Outline each blood parasite and name the species.
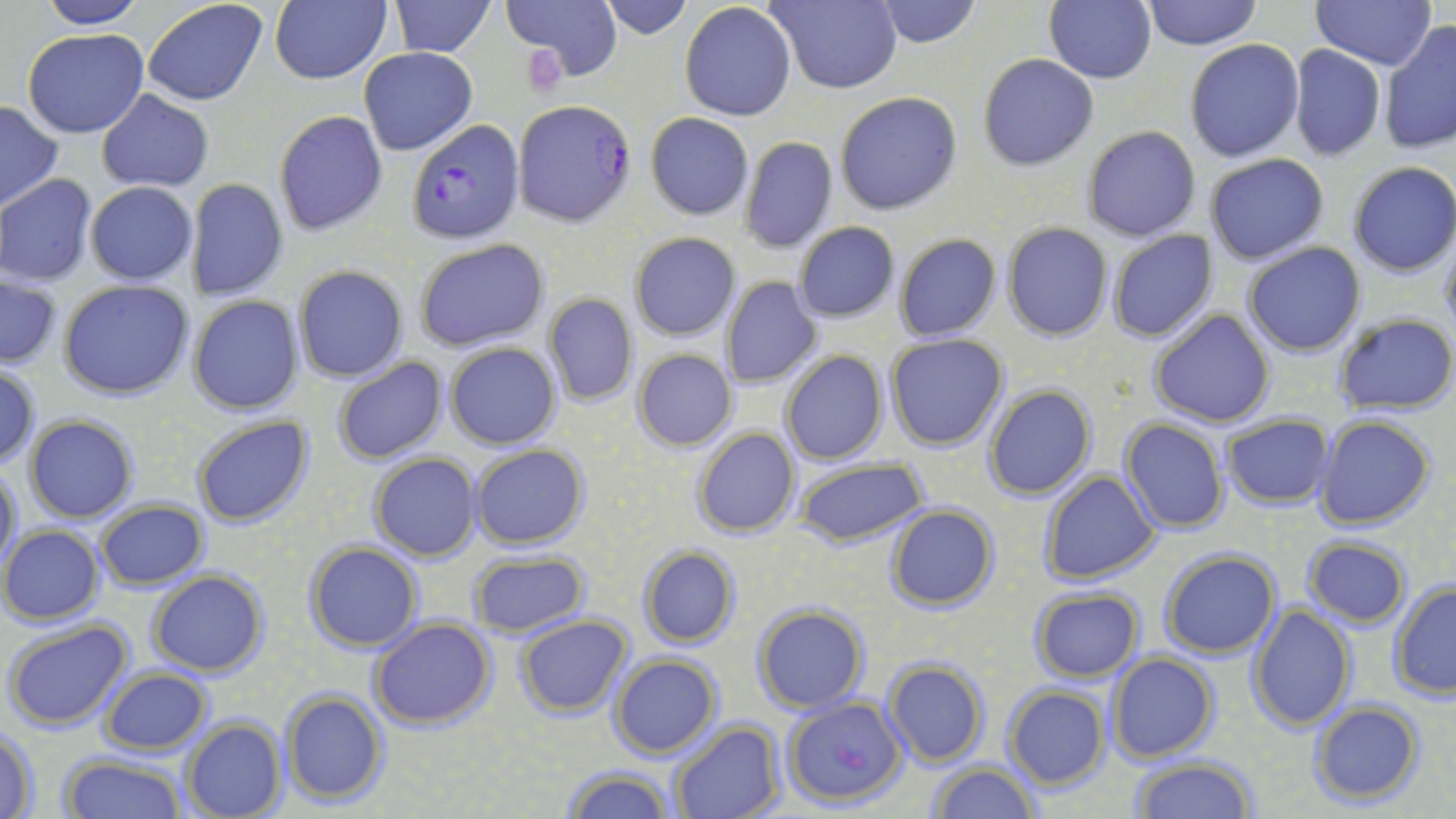

Approximate bounding boxes as (x1, y1, x2, y2) in pixels.
Plasmodium falciparum-infected red blood cells: (514, 102, 637, 227), (407, 117, 524, 246), (783, 695, 905, 809).
No Plasmodium ovale, Plasmodium malariae, Plasmodium vivax, Babesia divergens, or Trypanosoma brucei observed.

Summary:
  - Uninfected red blood cell locations: (34, 0, 147, 29), (141, 0, 269, 106), (270, 0, 391, 86), (503, 0, 620, 81), (596, 0, 695, 39), (767, 0, 901, 93), (870, 0, 983, 48), (1046, 0, 1158, 85), (1139, 0, 1261, 49), (1314, 0, 1434, 70), (388, 1, 496, 56), (679, 3, 797, 120), (1381, 20, 1455, 156), (23, 29, 149, 138), (1185, 38, 1306, 162), (1288, 44, 1386, 162), (359, 47, 478, 156), (977, 54, 1098, 171), (96, 89, 214, 193), (834, 91, 963, 215), (0, 100, 62, 212), (273, 109, 389, 237), (644, 112, 754, 220), (1081, 125, 1201, 242), (739, 135, 838, 253), (1205, 154, 1330, 265), (1345, 162, 1456, 278), (0, 174, 97, 286), (188, 177, 288, 302), (84, 181, 198, 285), (792, 221, 901, 323), (1001, 221, 1114, 342), (1106, 229, 1218, 343), (629, 233, 739, 341), (895, 233, 1001, 342), (1439, 233, 1456, 341), (414, 238, 549, 353), (1243, 241, 1365, 356), (294, 265, 409, 382), (1, 274, 62, 369), (721, 277, 822, 389), (60, 280, 194, 400), (543, 292, 639, 408), (189, 296, 305, 415), (1149, 309, 1276, 427), (1333, 313, 1456, 417), (885, 333, 1009, 451), (444, 342, 561, 450), (632, 348, 737, 451), (779, 350, 888, 465), (333, 357, 448, 464), (1, 367, 39, 468), (983, 385, 1097, 500), (1221, 414, 1335, 509), (24, 415, 139, 523), (191, 416, 313, 530), (1314, 416, 1437, 531), (1120, 417, 1230, 534), (691, 425, 802, 538), (471, 444, 588, 550), (367, 452, 482, 561), (793, 456, 927, 549), (1, 462, 21, 575), (1038, 470, 1163, 586), (94, 499, 210, 591), (885, 505, 998, 611), (1, 525, 104, 624), (1301, 536, 1413, 629), (304, 541, 422, 653), (638, 545, 740, 649), (465, 550, 591, 636), (1158, 550, 1282, 659), (149, 570, 267, 676), (1387, 580, 1456, 701), (1027, 587, 1145, 683), (752, 603, 870, 713), (1247, 606, 1357, 732), (515, 616, 633, 716), (2, 618, 134, 733), (368, 618, 495, 731), (609, 653, 722, 758), (1105, 653, 1219, 763), (882, 658, 991, 768), (99, 667, 211, 756), (1001, 684, 1111, 790), (279, 687, 389, 808), (1308, 700, 1427, 808), (180, 717, 286, 819), (666, 720, 784, 819), (1, 727, 40, 817), (59, 754, 186, 819), (1128, 758, 1260, 818), (928, 762, 1039, 818), (564, 765, 675, 819)
  - Slide-level diagnosis: Plasmodium falciparum
  - Modality: light microscopy
  - Magnification: 1000x
  - Preparation: thin blood film
  - Image size: 1456×819 pixels
  - Stain: May-Grünwald-Giemsa
  - Field of view: single